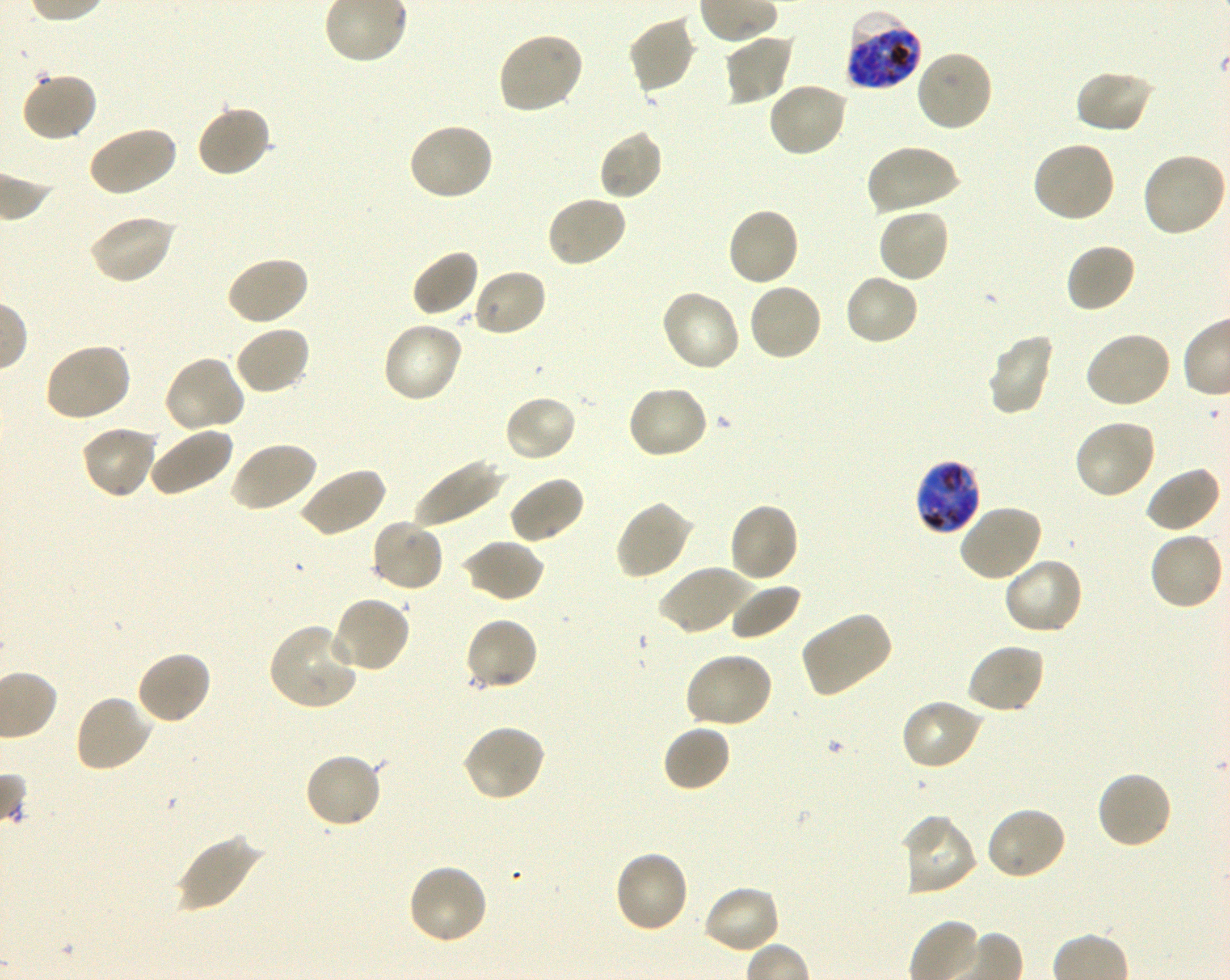

Not every red blood cell is marked. A life-cycle stage — or a range of stages, where the recorded stages span more than one — follows each staged infected red blood cell.
{
  "image_size": "1230×980 pixels",
  "culture": "in-vitro Plasmodium falciparum strain 3D7, shaking",
  "preparation": "thin blood smear",
  "locations_of_uninfected_red_blood_cells": "approximate bounding boxes as {x1, y1, x2, y2} in pixels: {627, 15, 697, 95}, {497, 31, 585, 115}, {723, 32, 795, 105}, {915, 48, 994, 133}, {1073, 69, 1155, 135}, {20, 72, 99, 143}, {766, 81, 851, 158}, {194, 104, 273, 179}, {407, 121, 495, 201}, {86, 124, 177, 198}, {598, 128, 664, 201}, {1030, 140, 1116, 224}, {866, 143, 960, 215}, {1141, 152, 1227, 238}, {545, 194, 628, 268}, {725, 206, 801, 287}, {876, 207, 951, 284}, {88, 214, 177, 286}, {1065, 242, 1137, 314}, {410, 248, 480, 318}, {226, 255, 310, 327}, {472, 268, 548, 338}, {842, 272, 921, 346}, {747, 281, 824, 361}, {659, 289, 741, 374}, {382, 320, 463, 404}, {233, 324, 312, 395}, {1084, 329, 1173, 409}, {986, 334, 1056, 417}, {42, 342, 132, 423}, {162, 355, 245, 435}, {626, 385, 709, 461}, {502, 395, 578, 463}, {1072, 418, 1156, 501}, {80, 425, 158, 500}, {146, 425, 234, 497}, {227, 440, 319, 513}, {412, 456, 503, 528}, {1142, 465, 1222, 534}, {296, 466, 386, 538}, {508, 476, 586, 545}, {615, 500, 693, 580}, {727, 502, 800, 584}, {957, 503, 1043, 583}, {370, 519, 445, 592}, {1148, 531, 1225, 612}, {462, 539, 545, 604}, {1002, 555, 1084, 635}, {657, 564, 751, 636}, {728, 583, 802, 641}, {328, 595, 411, 673}, {799, 611, 894, 697}, {463, 616, 539, 692}, {268, 621, 358, 710}, {964, 642, 1045, 715}, {134, 650, 213, 727}, {682, 652, 774, 730}, {72, 694, 155, 773}, {900, 699, 984, 772}, {462, 724, 547, 803}, {661, 724, 732, 793}, {303, 751, 384, 829}, {1095, 769, 1174, 850}, {984, 806, 1067, 882}, {897, 814, 978, 897}, {175, 834, 263, 913}, {612, 849, 690, 934}, {406, 863, 489, 947}, {702, 884, 783, 955}",
  "objective": "100x, oil immersion, numerical aperture 1.30",
  "donor_blood_group": "O+",
  "locations_of_infected_red_blood_cells": "approximate bounding boxes as {x1, y1, x2, y2} in pixels: {845, 10, 923, 91} late trophozoite to late schizont; {914, 458, 982, 535} early trophozoite to early schizont",
  "stain": "Giemsa",
  "field_of_view": "one from this slide"
}